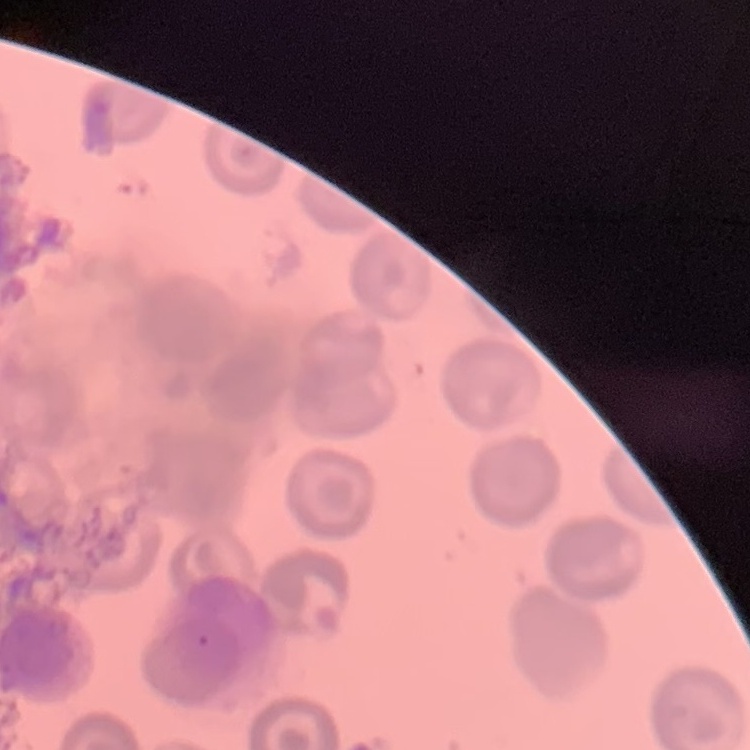

Summary:
  - Erythrocyte morphology: no rouleaux formation
  - Preparation: thin blood smear
  - Image type: one tile cut from a larger photomicrograph
  - Stain: Field's or Giemsa